Comment on the morphology of the red blood cells.
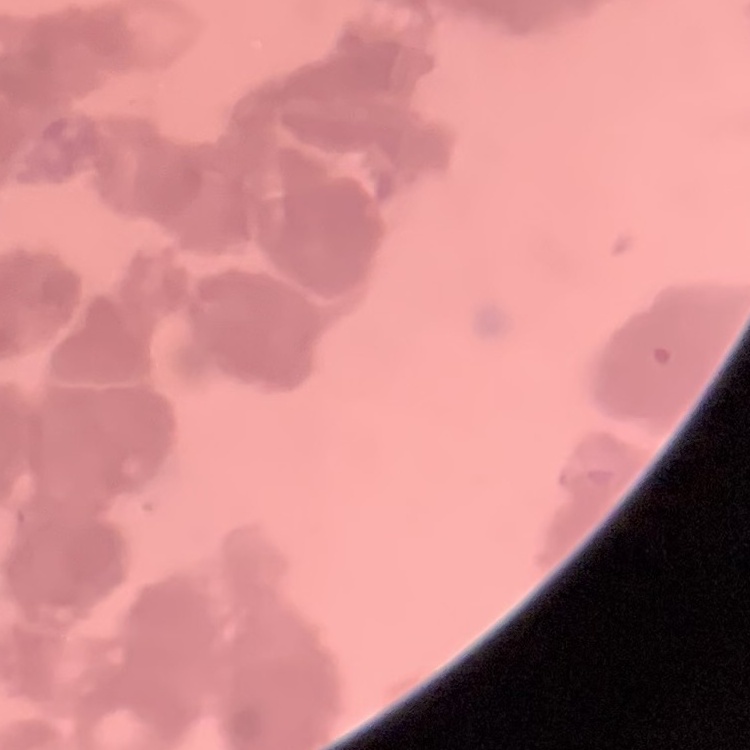
They show rouleaux formation.

preparation: thin blood smear
stain: Field's or Giemsa
image_type: one tile cut from a larger photomicrograph